Assess this cell for malaria.
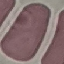
It is uninfected.

capture = smartphone through the microscope eyepiece
stain = Giemsa
preparation = thin blood smear
image type = automatically extracted cell patch, resized to 64 × 64 pixels